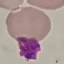

result: no malaria parasites detected
capture: smartphone camera at the microscope eyepiece
image_type: cell patch, automatically extracted from a larger field of view and resized to 64 × 64 pixels
stain: Giemsa
preparation: thin smear